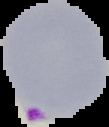
{
  "image_type": "segmented cell region on a black background",
  "result": "malaria parasites detected",
  "preparation": "thin blood film",
  "image_size": "109×127 pixels"
}